Describe the morphology of the red blood cells.
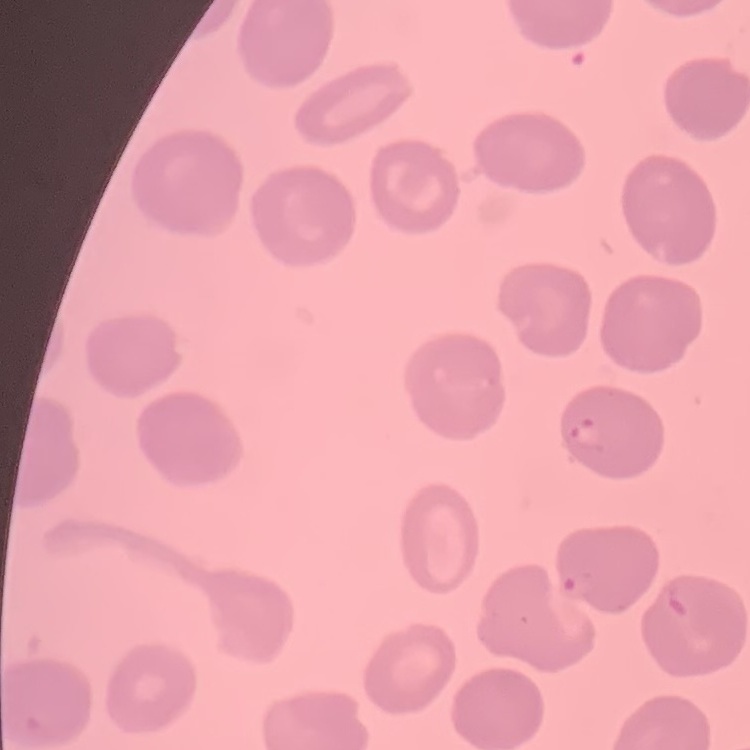
They show no rouleaux formation.

Summary:
  - Stain: Field's or Giemsa
  - Preparation: thin blood smear
  - Image type: one tile cut from a larger photomicrograph